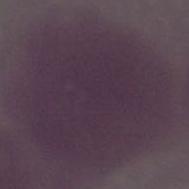 A red blood cell is shown. Micrograph. Captured at 1000x magnification.